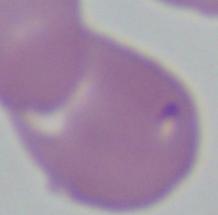

Photomicrograph. A Babesia parasite is shown. Captured at 1000x magnification.